Assess this cell for malaria.
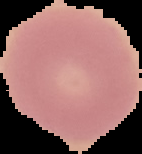

It is uninfected.

From a thin blood smear. Cell region segmented out of the field of view; the surrounding area is masked to black. Image is 142×154 pixels.